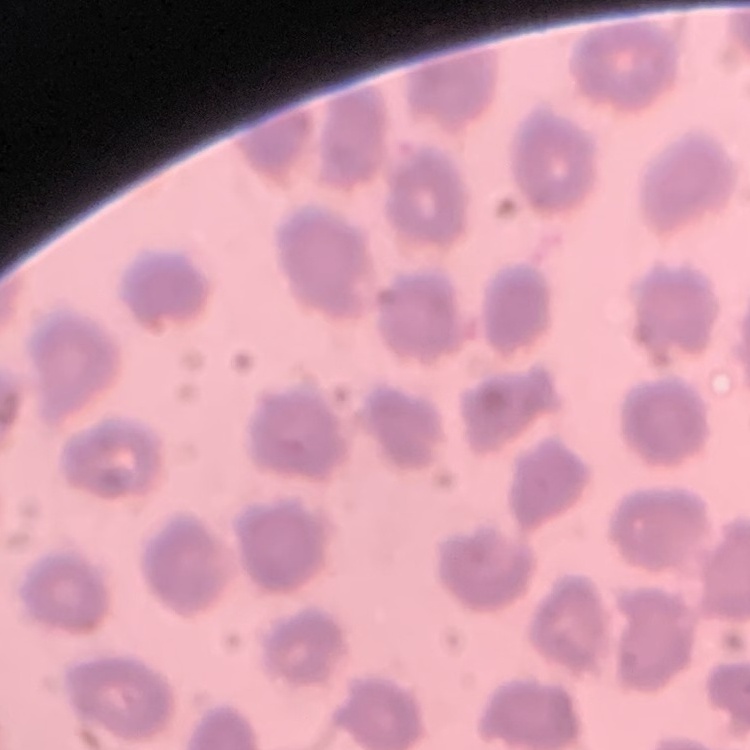

The erythrocytes show no rouleaux formation. Stained with either Field's or Giemsa. Thin blood smear. Square crop of a larger photomicrograph.